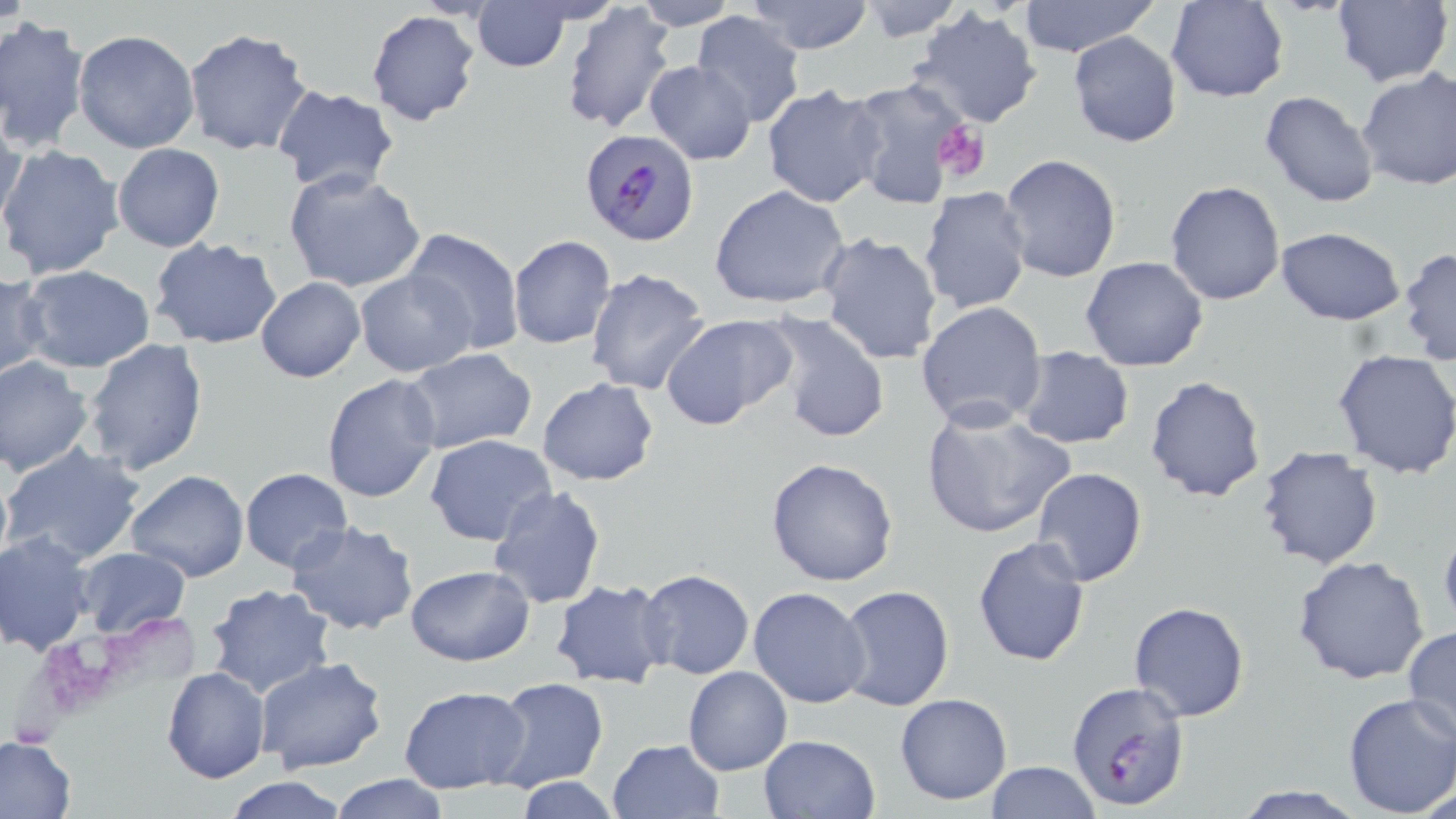

Summary:
  - Coordinate format: approximate bounding boxes as (x1, y1, x2, y2) in pixels
  - Uninfected red blood cell locations: (628, 0, 741, 30), (745, 0, 876, 53), (1164, 0, 1289, 103), (1334, 0, 1452, 87), (854, 1, 966, 42), (1016, 1, 1157, 57), (559, 2, 676, 135), (473, 3, 571, 72), (906, 5, 1043, 130), (366, 10, 483, 126), (690, 12, 809, 128), (0, 14, 90, 153), (183, 27, 311, 157), (73, 29, 202, 155), (1068, 31, 1182, 147), (643, 60, 757, 164), (1356, 68, 1456, 192), (842, 78, 977, 214), (762, 85, 888, 208), (272, 87, 400, 196), (1259, 89, 1379, 207), (1, 111, 27, 238), (112, 143, 225, 252), (0, 145, 126, 282), (998, 154, 1123, 283), (281, 168, 429, 296), (1164, 179, 1285, 305), (709, 185, 851, 309), (918, 187, 1034, 315), (1275, 226, 1406, 326), (404, 228, 524, 356), (818, 231, 944, 365), (508, 235, 617, 349), (149, 238, 284, 351), (1399, 246, 1456, 364), (1080, 257, 1209, 372), (21, 265, 156, 374), (584, 266, 712, 396), (355, 269, 475, 378), (0, 270, 48, 383), (256, 278, 366, 383), (915, 300, 1048, 432), (657, 312, 798, 430), (760, 312, 892, 443), (82, 338, 208, 476), (1014, 347, 1135, 449), (401, 349, 537, 456), (1332, 349, 1456, 479), (0, 356, 93, 476), (321, 374, 443, 505), (1145, 374, 1267, 501), (536, 379, 659, 486), (920, 403, 1075, 540), (426, 434, 557, 547), (3, 443, 146, 567), (1255, 446, 1383, 570), (0, 457, 12, 578), (765, 457, 898, 588), (1030, 467, 1146, 586), (239, 468, 354, 572), (125, 469, 249, 583), (486, 484, 605, 609), (284, 519, 422, 638), (1439, 519, 1456, 637), (1, 530, 95, 654), (973, 534, 1091, 668), (75, 547, 192, 639), (1292, 555, 1430, 686), (405, 565, 535, 666), (638, 569, 755, 680), (550, 579, 674, 690), (203, 583, 333, 699), (837, 584, 954, 712), (747, 586, 872, 709), (1129, 601, 1250, 722), (1402, 626, 1456, 751), (256, 656, 387, 774), (160, 666, 270, 783), (682, 667, 792, 775), (489, 677, 609, 791), (398, 686, 530, 793), (894, 692, 1013, 806), (1342, 692, 1456, 818), (758, 733, 879, 818), (0, 734, 77, 819), (607, 738, 725, 819), (984, 762, 1100, 818), (327, 774, 451, 818), (222, 775, 351, 817), (517, 777, 622, 818), (1231, 784, 1367, 818)
  - Plasmodium falciparum-infected red blood cell locations: (580, 128, 703, 247), (1064, 680, 1192, 812)
  - Platelet locations: (931, 119, 990, 183)
  - Slide-level diagnosis: Plasmodium falciparum
  - Stain: May-Grünwald-Giemsa
  - Image size: 1456×819 pixels
  - Modality: optical microscopy
  - Preparation: thin blood film
  - Magnification: 1000x
  - Field of view: one of a larger specimen